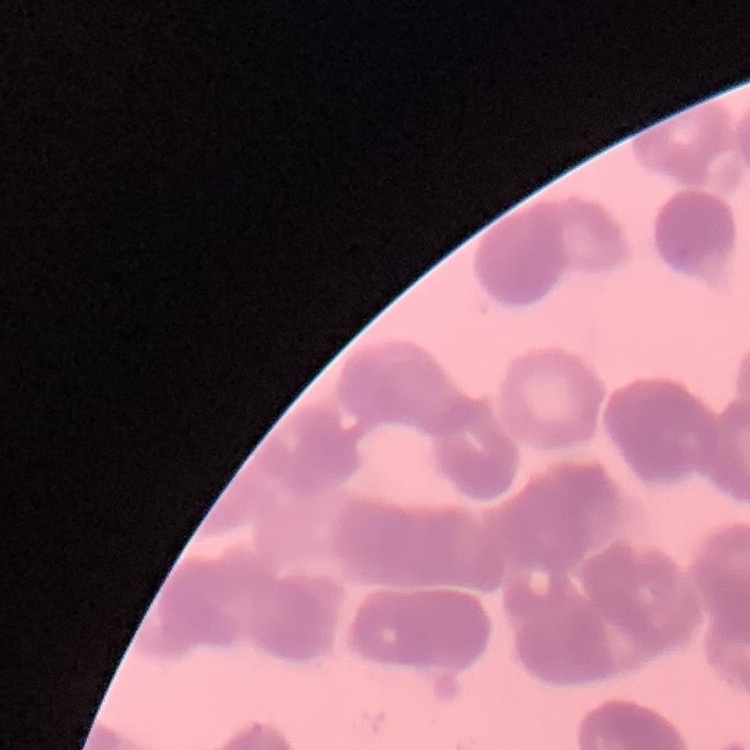

erythrocyte morphology = rouleaux formation
stain = Field's or Giemsa
preparation = thin blood film
image type = one tile cut from a larger photomicrograph